Comment on the morphology of the erythrocytes.
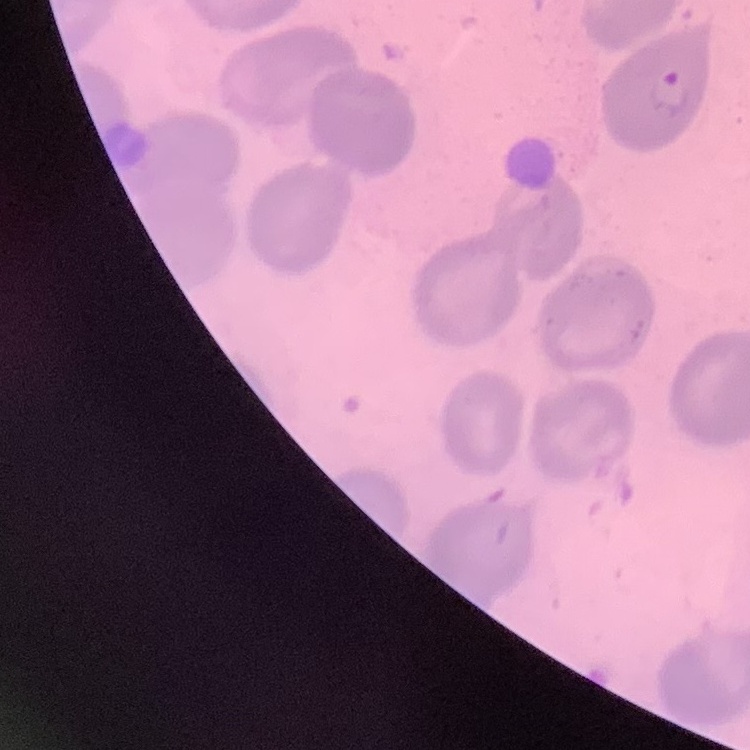
No rouleaux formation.

{
  "image_type": "one tile cut from a larger photomicrograph",
  "preparation": "thin peripheral smear",
  "stain": "Field's or Giemsa"
}